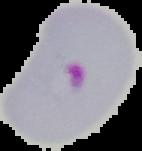
image type = cell region segmented out of the field of view; surrounding area masked to black
result = Plasmodium parasites detected
preparation = thin blood film
image size = 142×151 pixels